Comment on the morphology of the red blood cells.
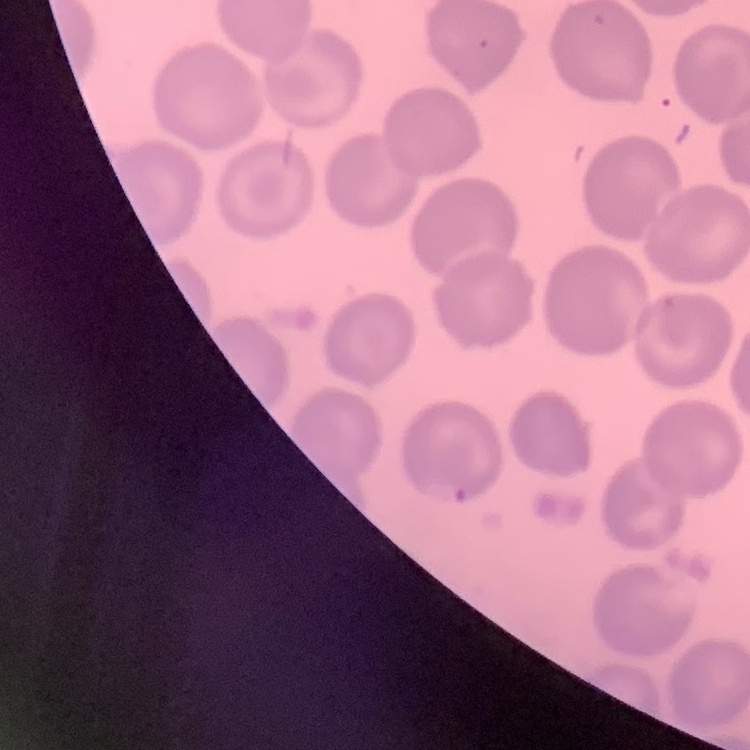
They show no rouleaux formation.

stain = Field's or Giemsa
image type = square crop of a larger photomicrograph
preparation = thin blood smear